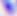

Summary:
  - Identification: Toxoplasma gondii
  - Magnification: 400x
  - Modality: micrograph